Locate every Plasmodium ovale-infected red blood cell.
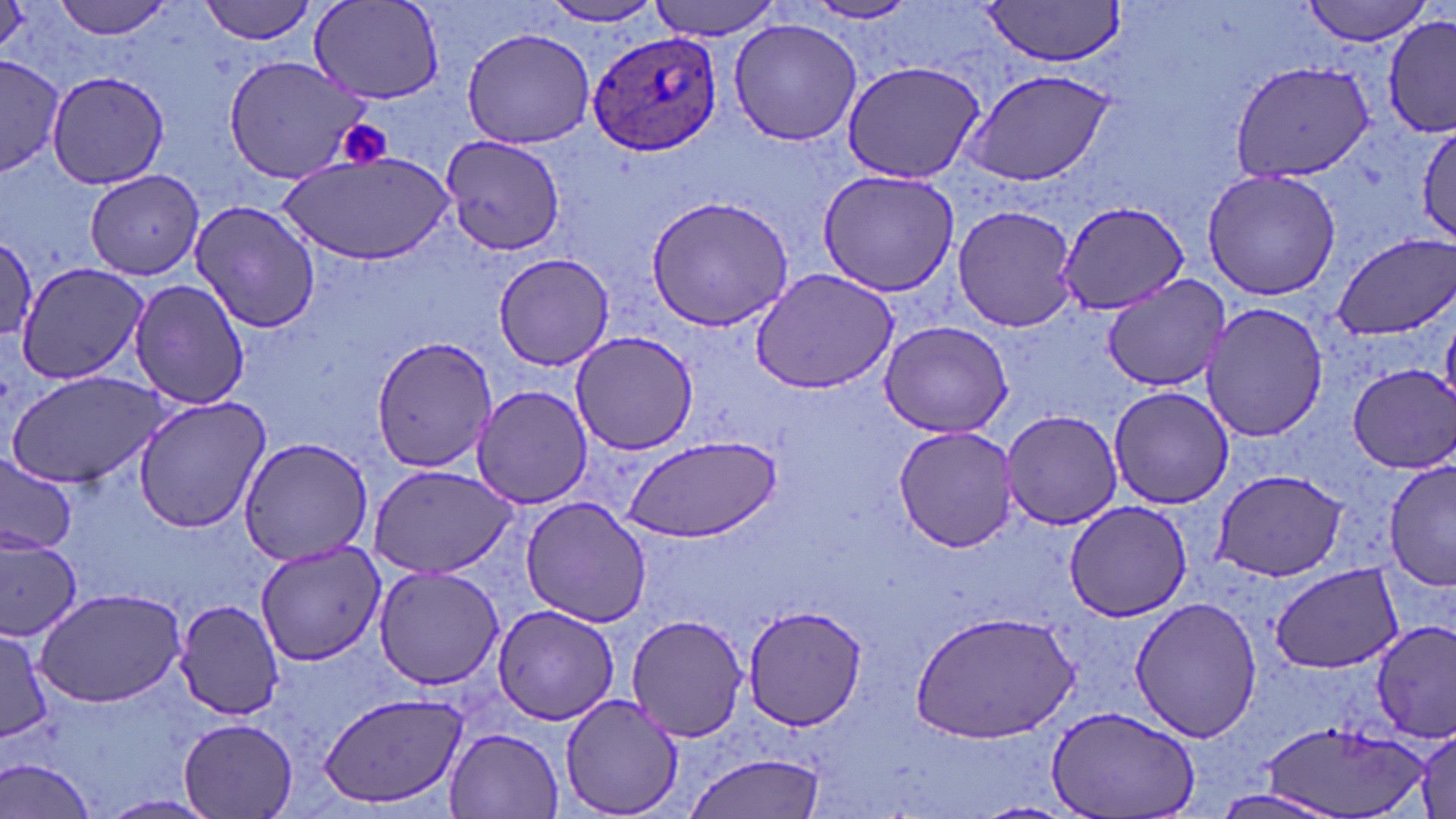
Approximate bounding boxes as named x1/y1/x2/y2 corners in pixels.
Plasmodium ovale-infected red blood cells: (x1=585, y1=30, x2=724, y2=158).

slide_level_diagnosis: Plasmodium ovale
field_of_view: single
modality: optical microscopy
stain: May-Grünwald-Giemsa
uninfected_red_blood_cell_locations: 'approximate bounding boxes as named x1/y1/x2/y2 corners in pixels: (x1=52, y1=0, x2=179, y2=40), (x1=198, y1=0, x2=321, y2=45), (x1=649, y1=0, x2=782, y2=39), (x1=1302, y1=0, x2=1433, y2=45), (x1=306, y1=1, x2=445, y2=105), (x1=538, y1=1, x2=666, y2=27), (x1=979, y1=1, x2=1127, y2=68), (x1=0, y1=2, x2=46, y2=61), (x1=802, y1=2, x2=920, y2=25), (x1=1382, y1=15, x2=1456, y2=137), (x1=727, y1=18, x2=862, y2=146), (x1=461, y1=27, x2=595, y2=150), (x1=0, y1=55, x2=63, y2=180), (x1=221, y1=55, x2=373, y2=184), (x1=840, y1=59, x2=987, y2=186), (x1=1229, y1=61, x2=1375, y2=185), (x1=959, y1=68, x2=1119, y2=188), (x1=45, y1=70, x2=173, y2=190), (x1=1415, y1=121, x2=1456, y2=243), (x1=440, y1=137, x2=564, y2=258), (x1=283, y1=151, x2=454, y2=264), (x1=1202, y1=167, x2=1340, y2=301), (x1=82, y1=169, x2=206, y2=279), (x1=816, y1=170, x2=959, y2=296), (x1=644, y1=195, x2=795, y2=332), (x1=189, y1=199, x2=321, y2=335), (x1=1056, y1=202, x2=1188, y2=316), (x1=953, y1=204, x2=1077, y2=333), (x1=1331, y1=234, x2=1456, y2=340), (x1=1, y1=236, x2=39, y2=348), (x1=492, y1=251, x2=614, y2=371), (x1=14, y1=262, x2=151, y2=387), (x1=749, y1=267, x2=900, y2=394), (x1=1099, y1=274, x2=1234, y2=390), (x1=129, y1=277, x2=250, y2=409), (x1=1201, y1=303, x2=1327, y2=444), (x1=878, y1=320, x2=1016, y2=438), (x1=571, y1=330, x2=698, y2=456), (x1=369, y1=335, x2=499, y2=474), (x1=1346, y1=363, x2=1456, y2=473), (x1=4, y1=370, x2=172, y2=490), (x1=471, y1=385, x2=592, y2=509), (x1=1107, y1=385, x2=1235, y2=510), (x1=133, y1=395, x2=271, y2=533), (x1=1001, y1=409, x2=1126, y2=531), (x1=892, y1=424, x2=1022, y2=553), (x1=620, y1=433, x2=782, y2=541), (x1=236, y1=436, x2=374, y2=565), (x1=0, y1=451, x2=77, y2=556), (x1=1383, y1=459, x2=1456, y2=593), (x1=368, y1=464, x2=518, y2=580), (x1=1210, y1=469, x2=1349, y2=582), (x1=520, y1=498, x2=653, y2=627), (x1=1063, y1=499, x2=1196, y2=622), (x1=0, y1=537, x2=83, y2=640), (x1=256, y1=542, x2=384, y2=664), (x1=1269, y1=562, x2=1401, y2=674), (x1=372, y1=565, x2=506, y2=690), (x1=34, y1=587, x2=188, y2=708), (x1=1129, y1=596, x2=1262, y2=743), (x1=174, y1=597, x2=285, y2=721), (x1=740, y1=604, x2=870, y2=731), (x1=491, y1=606, x2=621, y2=726), (x1=912, y1=609, x2=1080, y2=742), (x1=627, y1=612, x2=750, y2=742), (x1=1372, y1=619, x2=1456, y2=740), (x1=0, y1=627, x2=51, y2=745), (x1=318, y1=690, x2=469, y2=811), (x1=558, y1=693, x2=686, y2=818), (x1=1047, y1=701, x2=1202, y2=819), (x1=178, y1=715, x2=300, y2=818), (x1=1260, y1=718, x2=1431, y2=818), (x1=447, y1=727, x2=564, y2=818), (x1=1411, y1=728, x2=1455, y2=819), (x1=684, y1=751, x2=829, y2=819), (x1=3, y1=759, x2=100, y2=819), (x1=1209, y1=789, x2=1349, y2=819)'
image_size: 1456×819 pixels
platelet_locations: 'approximate bounding boxes as named x1/y1/x2/y2 corners in pixels: (x1=334, y1=119, x2=394, y2=170)'
magnification: 1000x
preparation: thin blood smear